Report the malaria status of this cell.
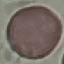
Uninfected.

preparation = thin smear
stain = Giemsa
capture = smartphone through the microscope eyepiece
image type = automatically extracted cell patch, resized to 64 × 64 pixels